Classify this cell by malaria status.
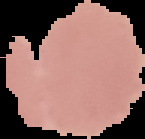
It is uninfected.

image size = 145×139 pixels
preparation = thin blood smear
image type = segmented cell region with the area outside set to black